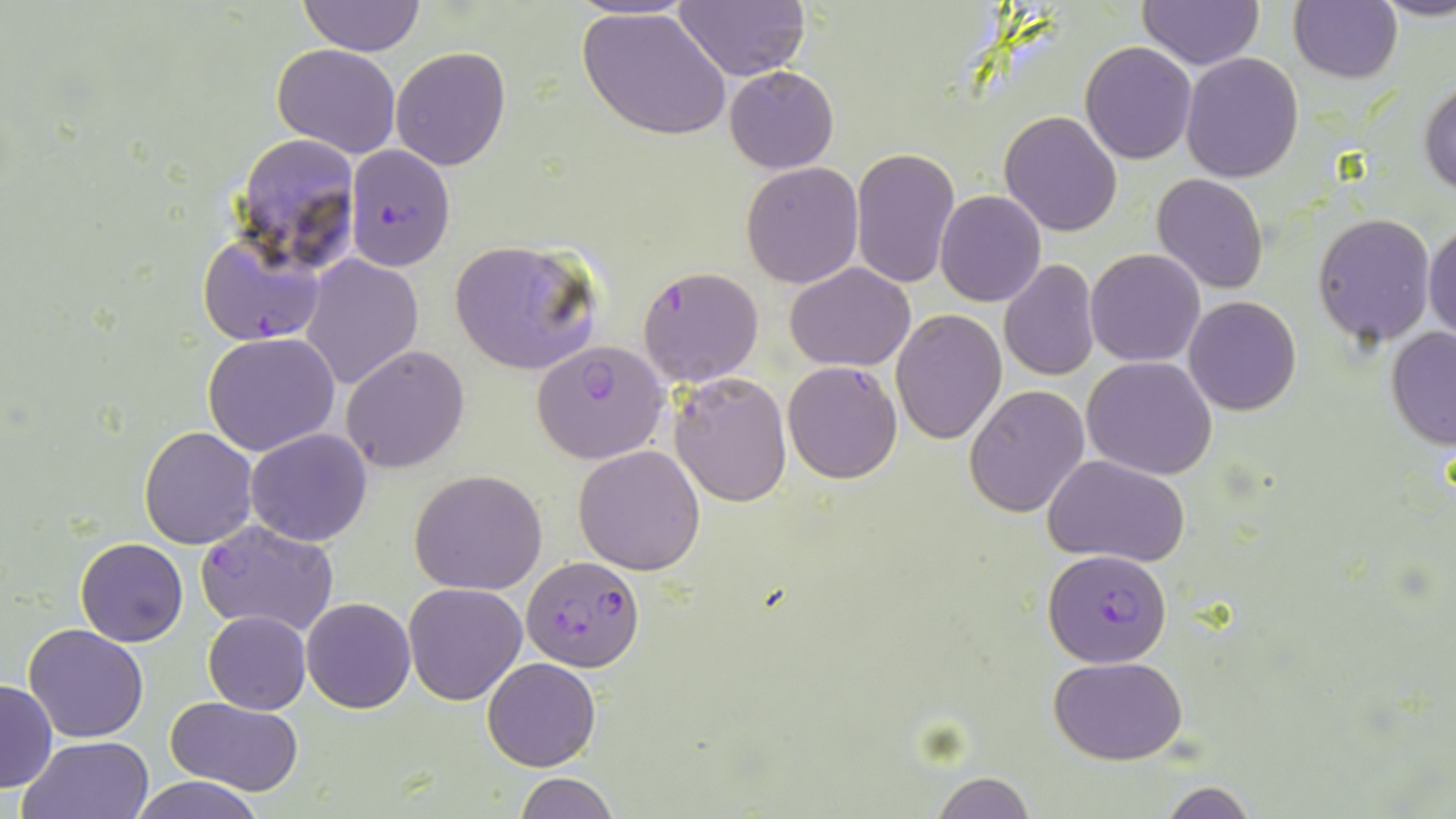

{
  "slide_level_diagnosis": "Plasmodium falciparum",
  "stain": "May-Grünwald-Giemsa",
  "uninfected_red_blood_cell_locations": "approximate bounding boxes as named x1/y1/x2/y2 corners in pixels: (x1=1137, y1=0, x2=1264, y2=70), (x1=1379, y1=0, x2=1456, y2=22), (x1=673, y1=1, x2=810, y2=81), (x1=1288, y1=1, x2=1401, y2=84), (x1=298, y1=2, x2=425, y2=55), (x1=577, y1=6, x2=731, y2=142), (x1=1080, y1=42, x2=1197, y2=164), (x1=272, y1=44, x2=402, y2=160), (x1=391, y1=47, x2=511, y2=170), (x1=1180, y1=52, x2=1305, y2=183), (x1=724, y1=65, x2=838, y2=173), (x1=1419, y1=73, x2=1456, y2=197), (x1=1000, y1=111, x2=1123, y2=238), (x1=232, y1=131, x2=362, y2=274), (x1=849, y1=146, x2=960, y2=290), (x1=740, y1=161, x2=864, y2=289), (x1=1151, y1=173, x2=1269, y2=294), (x1=935, y1=191, x2=1046, y2=307), (x1=1311, y1=212, x2=1438, y2=346), (x1=1425, y1=218, x2=1456, y2=346), (x1=448, y1=240, x2=602, y2=375), (x1=1085, y1=248, x2=1206, y2=366), (x1=300, y1=254, x2=425, y2=390), (x1=999, y1=258, x2=1099, y2=384), (x1=784, y1=262, x2=915, y2=370), (x1=1184, y1=295, x2=1301, y2=416), (x1=892, y1=309, x2=1005, y2=445), (x1=1384, y1=326, x2=1456, y2=449), (x1=203, y1=332, x2=341, y2=458), (x1=339, y1=344, x2=470, y2=474), (x1=1083, y1=357, x2=1218, y2=479), (x1=667, y1=371, x2=794, y2=506), (x1=964, y1=385, x2=1091, y2=518), (x1=138, y1=425, x2=259, y2=549), (x1=245, y1=428, x2=374, y2=547), (x1=574, y1=444, x2=707, y2=575), (x1=1045, y1=456, x2=1189, y2=567), (x1=409, y1=469, x2=549, y2=594), (x1=74, y1=538, x2=189, y2=647), (x1=403, y1=581, x2=528, y2=704), (x1=302, y1=597, x2=415, y2=713), (x1=203, y1=610, x2=311, y2=713), (x1=23, y1=623, x2=149, y2=743), (x1=1049, y1=655, x2=1188, y2=764), (x1=482, y1=656, x2=602, y2=771), (x1=0, y1=677, x2=56, y2=793), (x1=168, y1=696, x2=304, y2=794), (x1=19, y1=734, x2=154, y2=819), (x1=929, y1=772, x2=1037, y2=818), (x1=130, y1=774, x2=266, y2=819), (x1=513, y1=774, x2=619, y2=818), (x1=1159, y1=781, x2=1257, y2=818)",
  "modality": "optical microscopy",
  "preparation": "thin blood smear",
  "image_size": "1456×819 pixels",
  "plasmodium_falciparum_infected_red_blood_cell_locations": "approximate bounding boxes as named x1/y1/x2/y2 corners in pixels: (x1=344, y1=144, x2=458, y2=272), (x1=197, y1=230, x2=327, y2=345), (x1=637, y1=265, x2=764, y2=387), (x1=530, y1=340, x2=671, y2=465), (x1=783, y1=362, x2=903, y2=483), (x1=196, y1=519, x2=338, y2=637), (x1=1043, y1=547, x2=1173, y2=667), (x1=520, y1=556, x2=646, y2=672)",
  "magnification": "1000x",
  "field_of_view": "single"
}